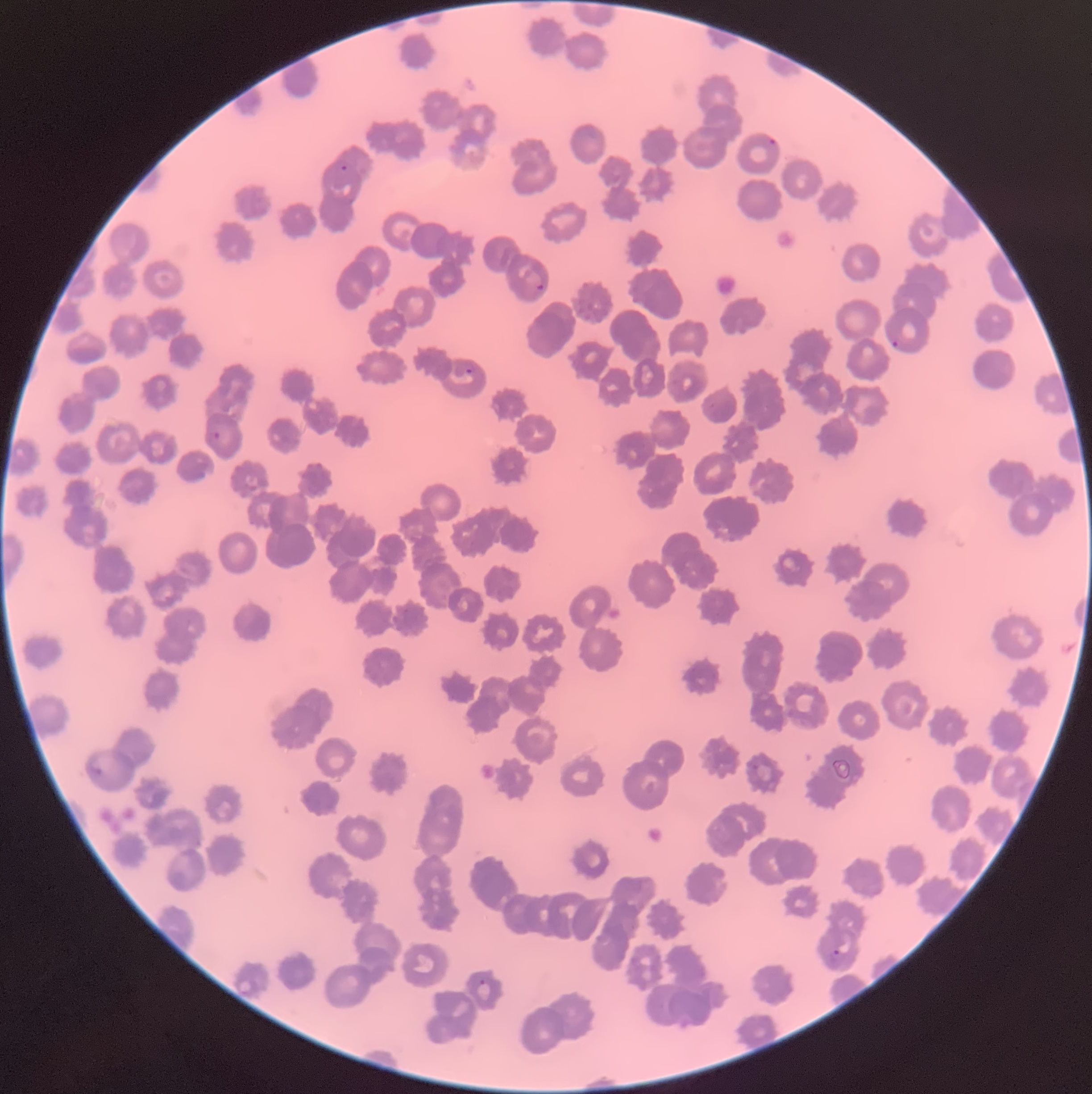

Approximate bounding boxes as named x1/y1/x2/y2 corners in pixels. Plasmodium parasite locations: (x1=769, y1=137, x2=777, y2=145), (x1=536, y1=283, x2=545, y2=291), (x1=891, y1=339, x2=899, y2=348), (x1=463, y1=361, x2=475, y2=375), (x1=212, y1=431, x2=222, y2=441), (x1=88, y1=761, x2=103, y2=775), (x1=828, y1=948, x2=844, y2=967), (x1=478, y1=979, x2=486, y2=986). Plasmodium parasites too small for a box (approximate object centers, named x/y in pixels): (x=343, y=167). Thin blood smear. Image is 1092×1094 pixels. Optical microscopy. The red blood cells show rouleaux formation.